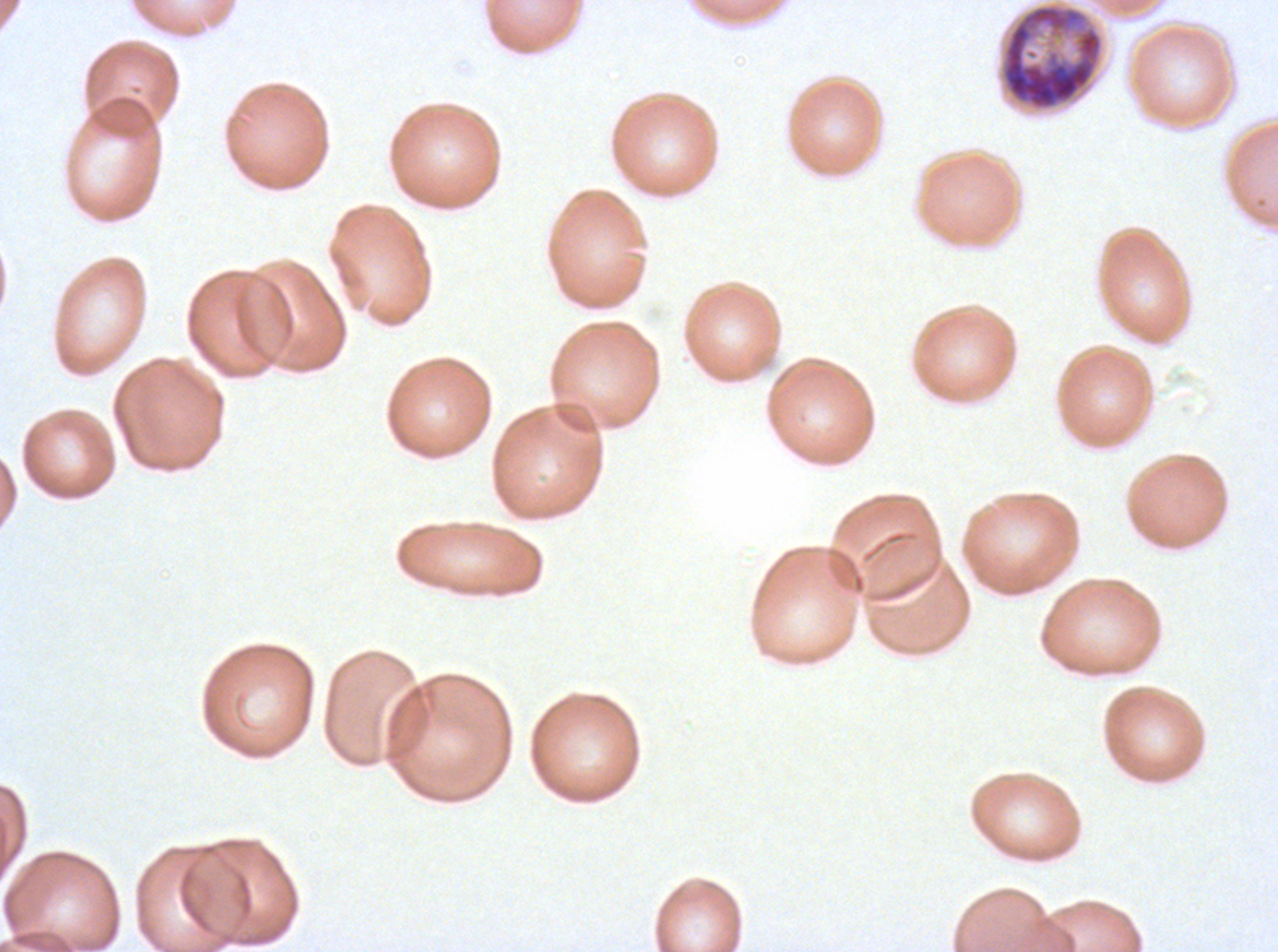 Approximate bounding boxes as {x1, y1, x2, y2} in pixels. Early schizont locations: {999, 3, 1104, 112}. A sub-image separated from a larger composite. Thin blood smear. P. falciparum cultured ex vivo for 24 to 48 hours, from a patient in The Gambia. Image is 1278×952 pixels. Giemsa-stained preparation.